Assess for malaria.
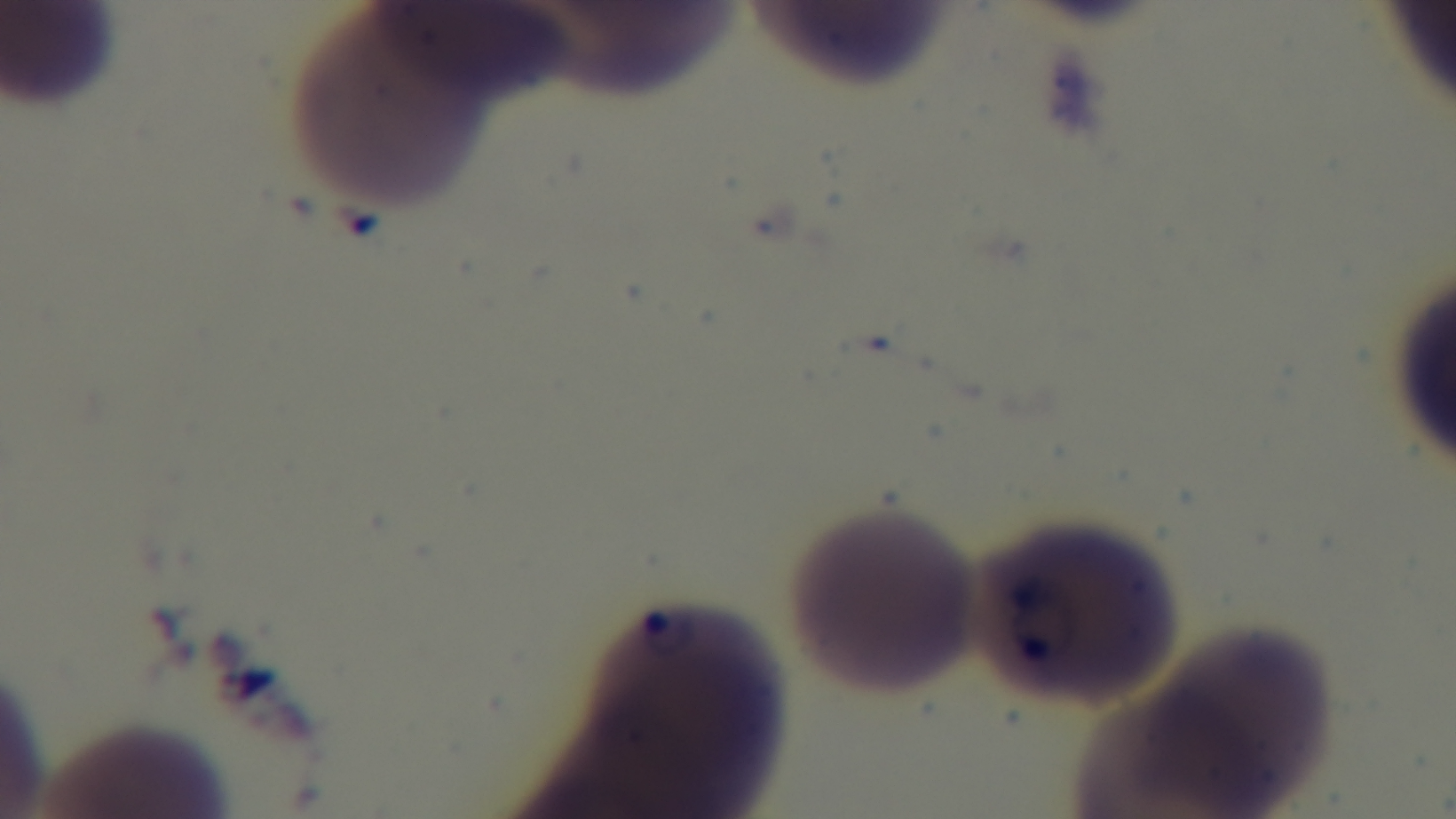

Infected.

Giemsa-stained. Single field of view. Mounted 4K digital camera. Preparation: thin smear. Photomicrograph. 100x oil-immersion objective.